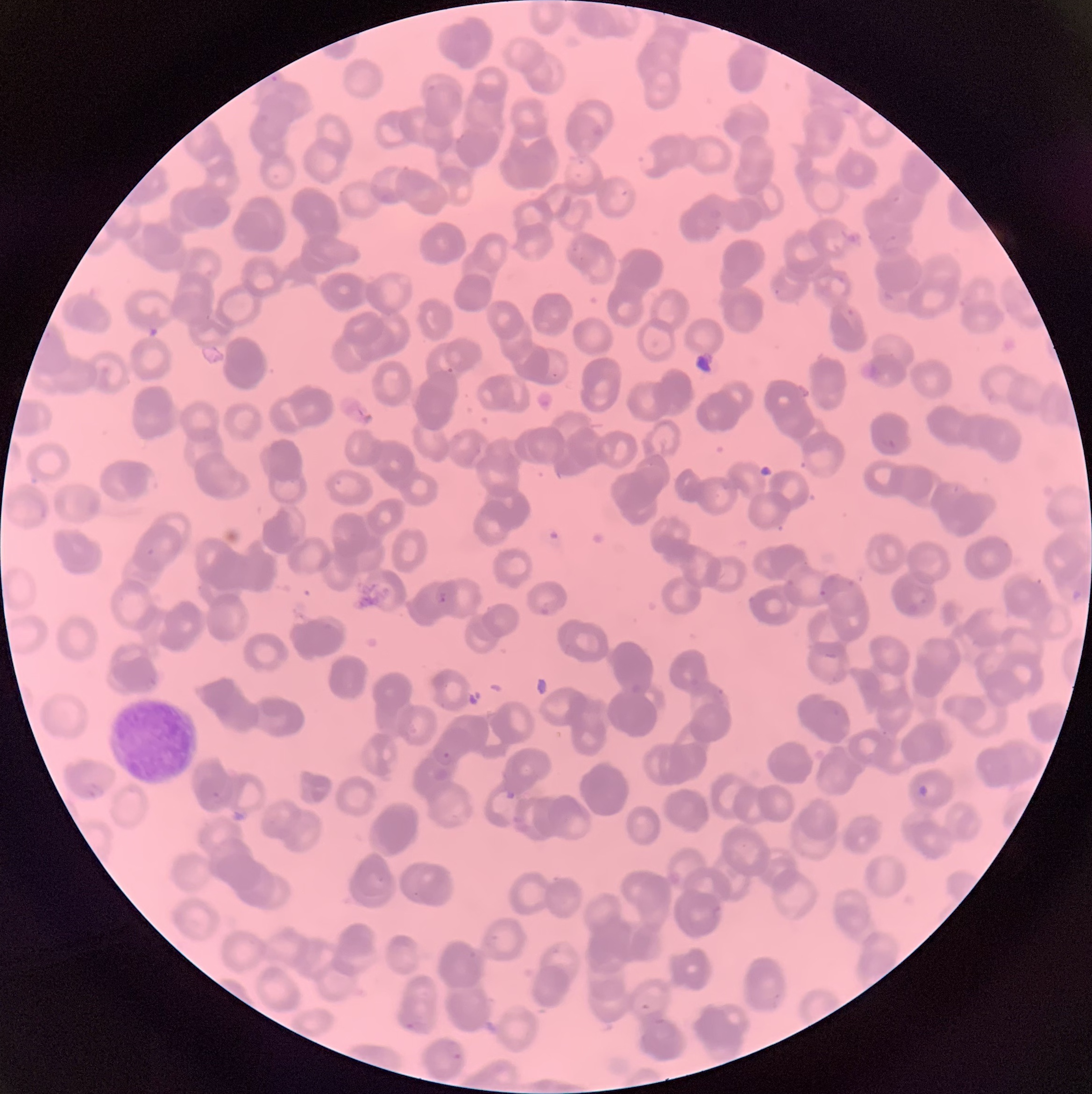

Summary:
  - Coordinate format: approximate bounding boxes as named x1/y1/x2/y2 corners in pixels
  - Plasmodium parasite locations: (x1=446, y1=366, x2=456, y2=375), (x1=438, y1=590, x2=448, y2=605), (x1=441, y1=751, x2=452, y2=760), (x1=85, y1=782, x2=105, y2=799), (x1=917, y1=783, x2=929, y2=798), (x1=505, y1=789, x2=517, y2=801), (x1=641, y1=1002, x2=653, y2=1013), (x1=403, y1=1021, x2=423, y2=1032), (x1=446, y1=1040, x2=464, y2=1064)
  - White blood cell locations: (x1=108, y1=694, x2=202, y2=785)
  - Preparation: thin blood film
  - Image size: 1092×1094 pixels
  - Modality: light microscopy
  - Red blood cell morphology: rouleaux formation